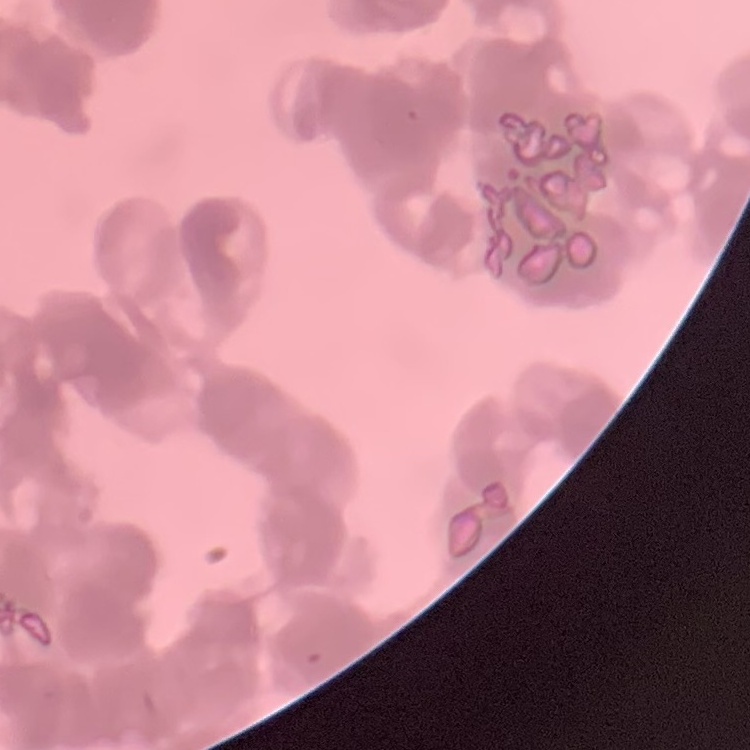
The erythrocytes show rouleaux formation. One tile cut from a larger photomicrograph. Stained with either Field's or Giemsa. Thin blood film.